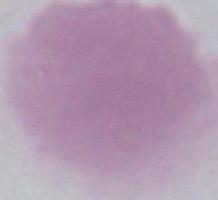

Summary:
  - Magnification: 1000x
  - Modality: photomicrograph
  - Identification: red blood cell